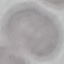
Malaria status: uninfected. Acquired by smartphone through the microscope eyepiece. Thin blood smear. Giemsa stain. Automatically extracted cell patch, resized to 64 × 64 pixels.